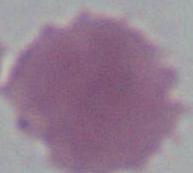
identification = erythrocyte
magnification = 1000x
modality = photomicrograph